Describe the morphology of the erythrocytes.
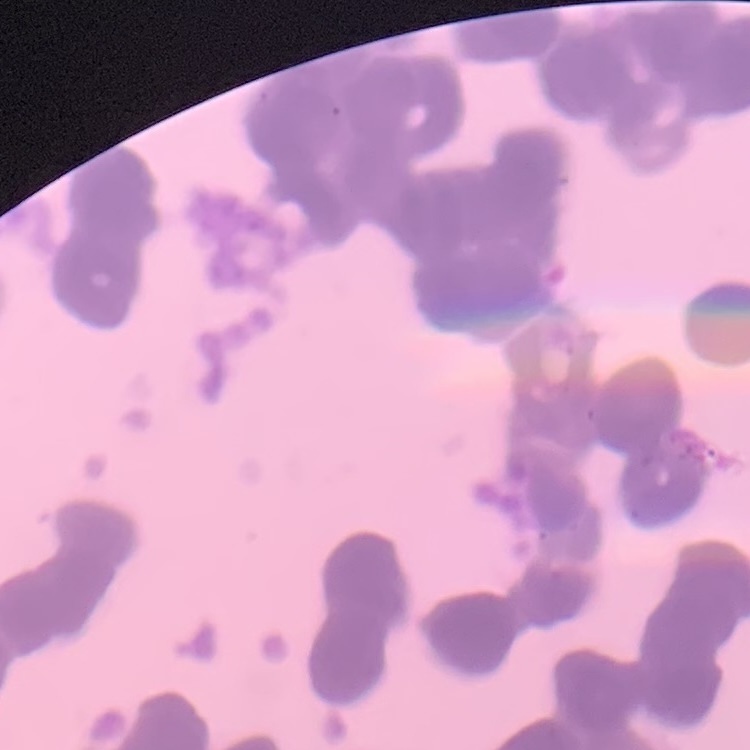

They show rouleaux formation.

Summary:
  - Preparation: thin blood film
  - Stain: Field's or Giemsa
  - Image type: one tile cut from a larger photomicrograph